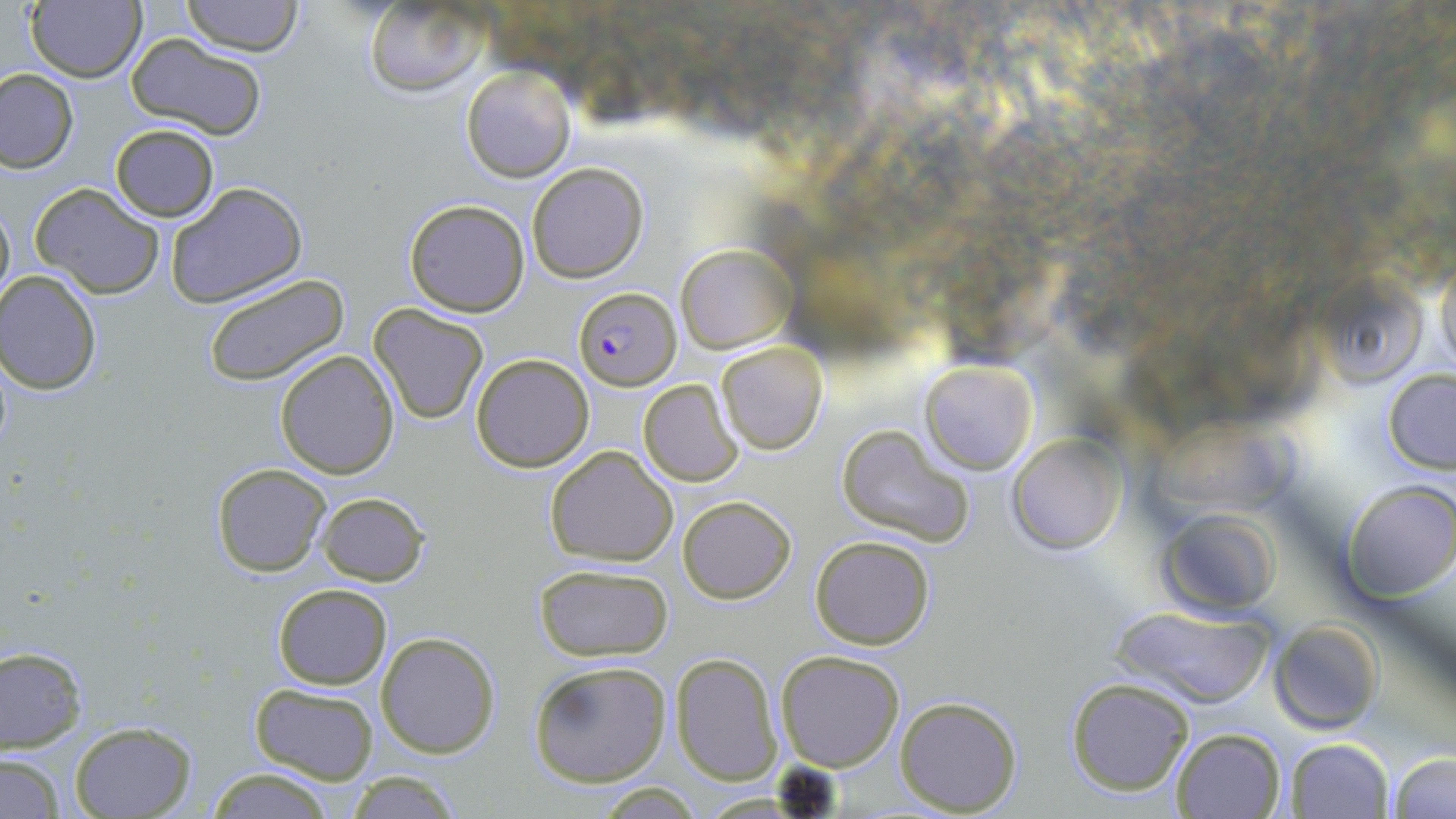

slide_level_diagnosis: Plasmodium falciparum
magnification: 1000x
preparation: thin blood film
field_of_view: one of a larger specimen
plasmodium_falciparum_infected_red_blood_cell_locations: 'approximate bounding boxes as (x1,y1)-(x2,y2) corner pairs in pixels: (574,287)-(679,390)'
modality: optical microscopy
uninfected_red_blood_cell_locations: 'approximate bounding boxes as (x1,y1)-(x2,y2) corner pairs in pixels: (182,0)-(302,55), (25,1)-(146,82), (363,2)-(487,95), (127,34)-(267,139), (460,64)-(575,184), (0,67)-(78,174), (110,124)-(219,222), (526,162)-(649,283), (165,182)-(306,309), (29,183)-(165,299), (0,194)-(14,311), (403,199)-(531,317), (677,246)-(795,353), (1433,248)-(1456,376), (202,271)-(351,388), (1,273)-(102,394), (1317,273)-(1426,385), (368,303)-(490,425), (716,341)-(828,455), (275,349)-(400,479), (470,354)-(595,473), (919,359)-(1037,474), (1383,368)-(1456,473), (638,379)-(745,487), (1154,412)-(1311,519), (835,423)-(974,549), (1006,435)-(1125,555), (545,445)-(679,566), (212,462)-(331,577), (1342,481)-(1456,602), (316,491)-(429,587), (678,495)-(796,604), (1156,508)-(1283,618), (810,535)-(938,649), (534,564)-(673,662), (272,583)-(393,690), (1108,603)-(1277,709), (1270,620)-(1383,733), (1080,627)-(1257,776), (375,630)-(501,758), (1,645)-(88,752), (775,649)-(904,771), (670,652)-(783,786), (528,659)-(672,787), (1064,676)-(1195,798), (248,682)-(380,784), (893,694)-(1022,815), (67,720)-(197,818), (1170,728)-(1286,818), (1283,738)-(1394,819), (1,752)-(64,817), (1386,752)-(1454,819), (202,766)-(340,819), (341,770)-(466,819)'
stain: May-Grünwald-Giemsa
image_size: 1456×819 pixels